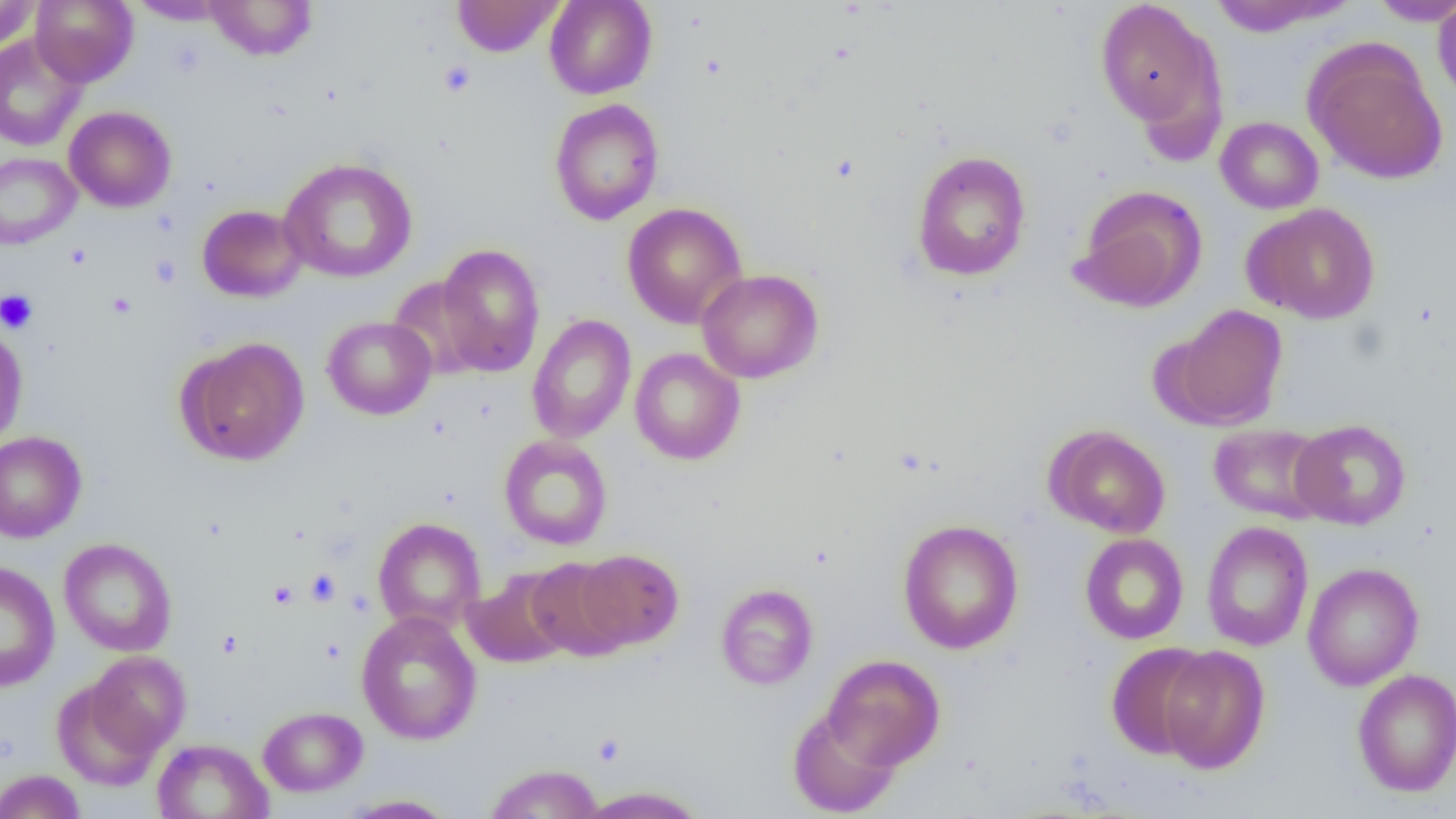

Summary:
  - Coordinate format: approximate bounding boxes as [x1, y1, x2, y2] in pixels
  - Uninfected red blood cell locations: [0, 0, 42, 52], [30, 0, 138, 87], [203, 0, 318, 61], [452, 0, 563, 57], [544, 0, 657, 99], [1095, 0, 1225, 134], [129, 1, 230, 25], [1205, 1, 1355, 36], [1367, 1, 1456, 26], [1433, 1, 1456, 105], [0, 33, 88, 151], [1304, 43, 1448, 185], [549, 99, 664, 226], [63, 106, 176, 212], [1215, 116, 1323, 214], [912, 150, 1031, 282], [0, 152, 81, 249], [279, 157, 417, 283], [1073, 185, 1207, 313], [622, 202, 748, 328], [1243, 203, 1380, 324], [197, 204, 307, 302], [436, 243, 546, 377], [697, 268, 824, 384], [387, 275, 492, 381], [1165, 305, 1289, 430], [526, 314, 636, 444], [322, 316, 436, 420], [0, 323, 28, 450], [527, 329, 745, 450], [179, 337, 309, 466], [630, 348, 745, 465], [1289, 419, 1412, 530], [1208, 423, 1332, 524], [1046, 426, 1170, 538], [0, 431, 87, 543], [499, 435, 613, 550], [372, 517, 486, 633], [897, 518, 1024, 655], [1201, 521, 1314, 651], [1080, 533, 1189, 644], [59, 537, 177, 656], [575, 548, 683, 650], [525, 557, 631, 661], [1, 561, 60, 691], [1302, 562, 1424, 691], [463, 568, 573, 668], [715, 583, 818, 690], [356, 611, 482, 745], [1106, 642, 1213, 759], [1158, 645, 1270, 774], [85, 651, 190, 757], [823, 654, 945, 770], [1352, 668, 1456, 796], [52, 679, 162, 789], [257, 706, 368, 796], [787, 706, 902, 817], [151, 738, 272, 819], [484, 763, 604, 819], [0, 769, 86, 819], [575, 786, 710, 818], [340, 795, 459, 818]
  - Platelet locations: [438, 59, 476, 97], [149, 254, 181, 288], [0, 289, 38, 334], [306, 568, 341, 606], [268, 580, 299, 610]
  - Slide-level diagnosis: negative for blood parasites
  - Magnification: 1000x
  - Image size: 1456×819 pixels
  - Modality: light microscopy
  - Preparation: thin blood film
  - Field of view: single